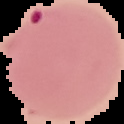

image size = 124×124 pixels
preparation = thin blood smear
result = Plasmodium parasites detected
image type = segmented cell region with the area outside set to black